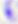

Summary:
  - Identification: Toxoplasma gondii
  - Magnification: 400x
  - Modality: photomicrograph